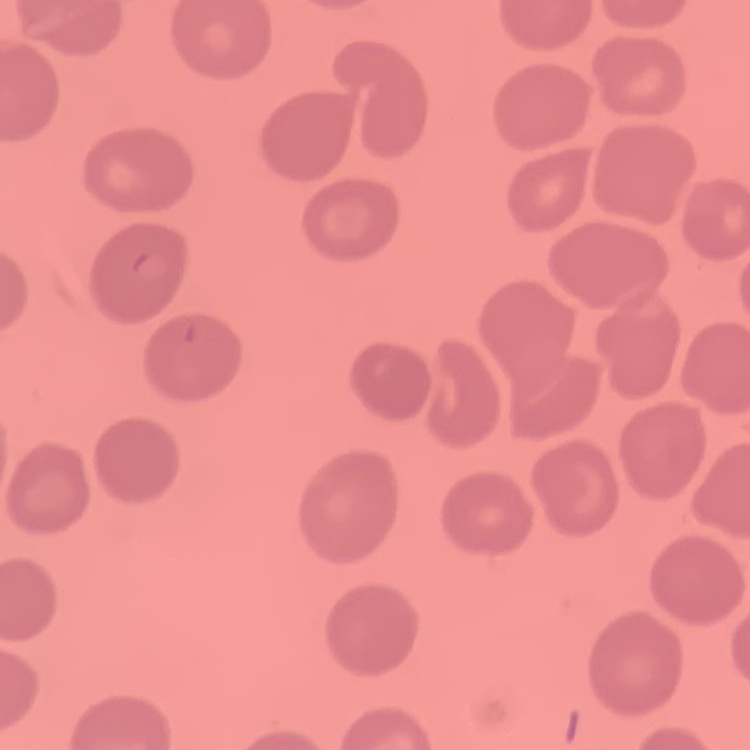

Summary:
  - Erythrocyte morphology: no rouleaux formation
  - Image type: one tile cut from a larger photomicrograph
  - Preparation: thin blood smear
  - Stain: Field's or Giemsa